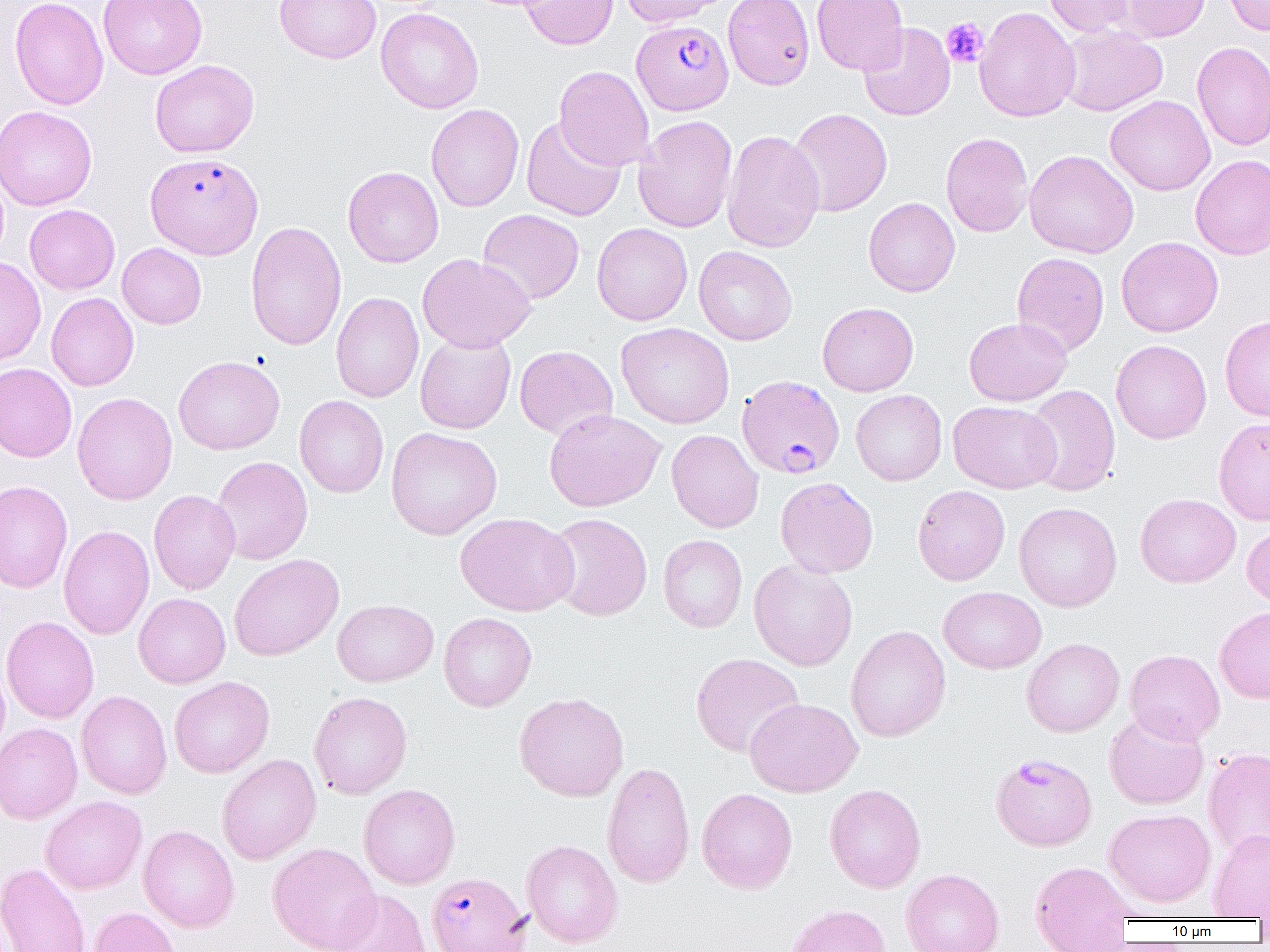 Approximate bounding boxes as named x1/y1/x2/y2 corners in pixels. Plasmodium falciparum-infected red blood cell locations: (x1=632, y1=20, x2=733, y2=115), (x1=146, y1=152, x2=263, y2=259), (x1=736, y1=375, x2=845, y2=479), (x1=991, y1=752, x2=1097, y2=850), (x1=426, y1=872, x2=531, y2=952). Uninfected red blood cell locations: (x1=9, y1=0, x2=108, y2=110), (x1=98, y1=0, x2=208, y2=79), (x1=274, y1=0, x2=381, y2=64), (x1=520, y1=0, x2=618, y2=50), (x1=621, y1=0, x2=727, y2=27), (x1=723, y1=0, x2=815, y2=90), (x1=811, y1=0, x2=909, y2=74), (x1=1043, y1=0, x2=1137, y2=38), (x1=1111, y1=0, x2=1212, y2=42), (x1=1222, y1=0, x2=1270, y2=36), (x1=975, y1=6, x2=1080, y2=122), (x1=376, y1=8, x2=484, y2=114), (x1=858, y1=22, x2=956, y2=121), (x1=1057, y1=24, x2=1168, y2=116), (x1=1192, y1=41, x2=1270, y2=151), (x1=150, y1=59, x2=259, y2=157), (x1=554, y1=65, x2=655, y2=171), (x1=1105, y1=95, x2=1215, y2=196), (x1=426, y1=104, x2=524, y2=212), (x1=0, y1=105, x2=97, y2=211), (x1=787, y1=108, x2=893, y2=217), (x1=634, y1=115, x2=737, y2=233), (x1=521, y1=116, x2=626, y2=221), (x1=722, y1=129, x2=824, y2=253), (x1=941, y1=132, x2=1033, y2=237), (x1=1024, y1=149, x2=1139, y2=258), (x1=1190, y1=154, x2=1270, y2=260), (x1=343, y1=166, x2=444, y2=268), (x1=863, y1=197, x2=960, y2=297), (x1=24, y1=204, x2=120, y2=294), (x1=478, y1=209, x2=584, y2=305), (x1=245, y1=221, x2=347, y2=351), (x1=592, y1=223, x2=693, y2=325), (x1=1116, y1=236, x2=1223, y2=337), (x1=117, y1=243, x2=207, y2=329), (x1=694, y1=245, x2=797, y2=346), (x1=1012, y1=252, x2=1109, y2=356), (x1=417, y1=253, x2=536, y2=352), (x1=0, y1=257, x2=46, y2=366), (x1=331, y1=292, x2=424, y2=403), (x1=46, y1=293, x2=138, y2=391), (x1=817, y1=302, x2=918, y2=396), (x1=1220, y1=315, x2=1270, y2=422), (x1=963, y1=317, x2=1072, y2=406), (x1=616, y1=322, x2=735, y2=429), (x1=415, y1=331, x2=516, y2=434), (x1=1111, y1=339, x2=1212, y2=444), (x1=514, y1=345, x2=618, y2=440), (x1=174, y1=355, x2=285, y2=455), (x1=0, y1=363, x2=77, y2=462), (x1=1023, y1=383, x2=1121, y2=497), (x1=850, y1=389, x2=947, y2=486), (x1=72, y1=392, x2=177, y2=504), (x1=294, y1=395, x2=389, y2=498), (x1=948, y1=400, x2=1061, y2=494), (x1=544, y1=409, x2=665, y2=512), (x1=1213, y1=417, x2=1270, y2=525), (x1=385, y1=427, x2=502, y2=540), (x1=666, y1=429, x2=764, y2=533), (x1=211, y1=455, x2=313, y2=565), (x1=775, y1=476, x2=879, y2=578), (x1=0, y1=480, x2=73, y2=594), (x1=912, y1=485, x2=1010, y2=585), (x1=149, y1=490, x2=240, y2=594), (x1=1135, y1=493, x2=1241, y2=588), (x1=1013, y1=502, x2=1122, y2=612), (x1=455, y1=512, x2=579, y2=616), (x1=546, y1=512, x2=652, y2=621), (x1=1241, y1=522, x2=1270, y2=609), (x1=58, y1=525, x2=154, y2=640), (x1=658, y1=535, x2=747, y2=632), (x1=229, y1=553, x2=344, y2=660), (x1=749, y1=559, x2=858, y2=671), (x1=938, y1=586, x2=1046, y2=674), (x1=133, y1=593, x2=231, y2=688), (x1=332, y1=599, x2=438, y2=687), (x1=1214, y1=606, x2=1270, y2=704), (x1=439, y1=612, x2=536, y2=712), (x1=1, y1=616, x2=99, y2=724), (x1=845, y1=625, x2=950, y2=742), (x1=1022, y1=638, x2=1124, y2=737), (x1=1125, y1=649, x2=1225, y2=745), (x1=690, y1=653, x2=805, y2=758), (x1=0, y1=659, x2=11, y2=760), (x1=169, y1=676, x2=274, y2=778), (x1=76, y1=690, x2=172, y2=799), (x1=308, y1=691, x2=413, y2=800), (x1=514, y1=691, x2=629, y2=802), (x1=745, y1=698, x2=863, y2=798), (x1=1104, y1=711, x2=1209, y2=810), (x1=0, y1=723, x2=82, y2=823), (x1=1203, y1=747, x2=1270, y2=859), (x1=217, y1=754, x2=321, y2=865), (x1=602, y1=760, x2=695, y2=889), (x1=825, y1=783, x2=926, y2=893), (x1=358, y1=784, x2=460, y2=889), (x1=697, y1=788, x2=798, y2=893), (x1=40, y1=796, x2=147, y2=894), (x1=1104, y1=808, x2=1216, y2=908), (x1=138, y1=825, x2=239, y2=932), (x1=1208, y1=829, x2=1270, y2=919), (x1=521, y1=839, x2=623, y2=948), (x1=268, y1=842, x2=381, y2=952), (x1=1029, y1=860, x2=1137, y2=952), (x1=0, y1=862, x2=91, y2=952), (x1=900, y1=868, x2=1004, y2=952), (x1=331, y1=890, x2=433, y2=952), (x1=784, y1=904, x2=892, y2=952), (x1=88, y1=906, x2=182, y2=952). Platelet locations: (x1=941, y1=17, x2=988, y2=68). Slide-level diagnosis: Plasmodium falciparum. Light microscopy. 1000x magnification. Image is 1270×952 pixels. Thin blood smear. Single field of view.